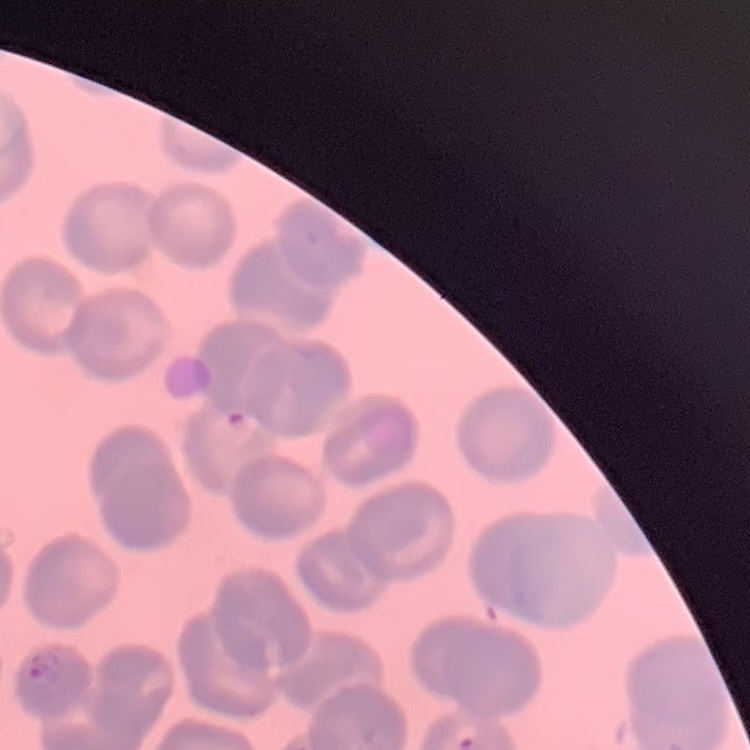

{
  "erythrocyte_morphology": "no rouleaux formation",
  "preparation": "thin peripheral smear",
  "stain": "Field's or Giemsa",
  "image_type": "one tile cut from a larger photomicrograph"
}